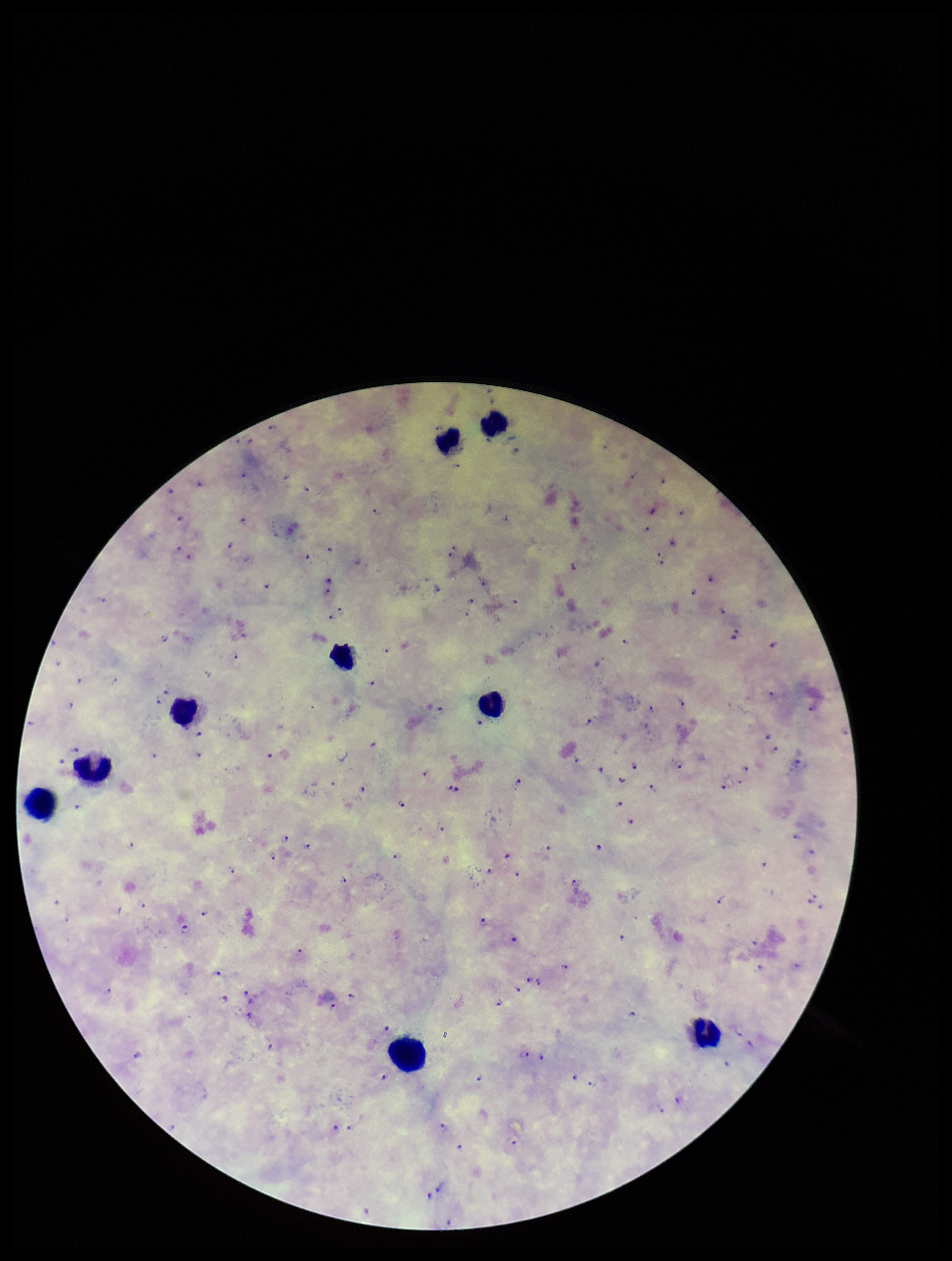
Species reported for this patient: Plasmodium falciparum. Leukocyte count: 9. Smartphone photograph taken through the eyepiece of a microscope. Plasmodium parasites: identified. Patient malaria status: positive. Preparation: thick smear. Giemsa stain. One field from this slide. Image is 952×1261 pixels. Parasite count: 110.